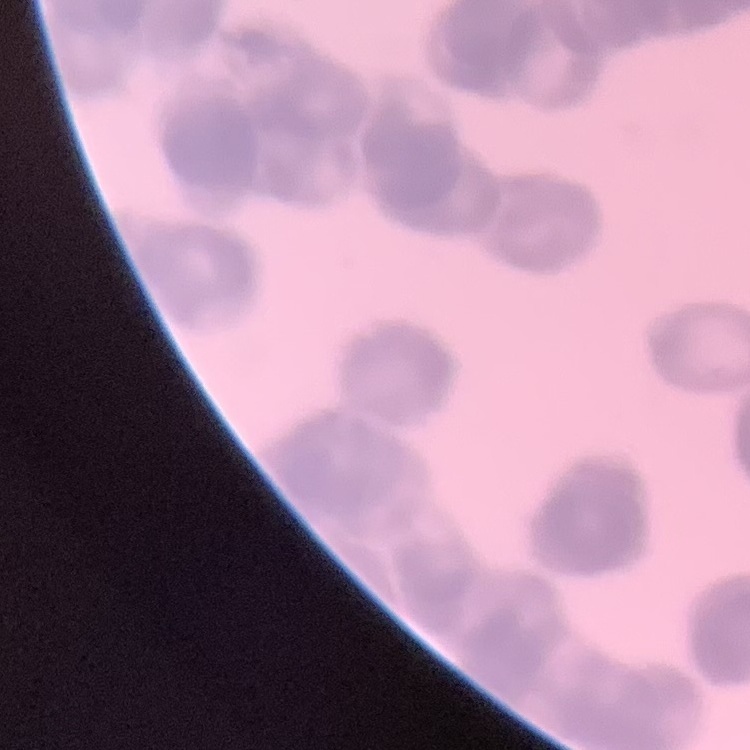

The red blood cells show rouleaux formation. Field's or Giemsa stain. Thin blood film. Square crop of a larger photomicrograph.